Assess this cell for malaria.
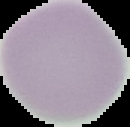

It is uninfected.

image type = cell region segmented out of the field of view; surrounding area masked to black
preparation = thin blood smear
image size = 130×127 pixels